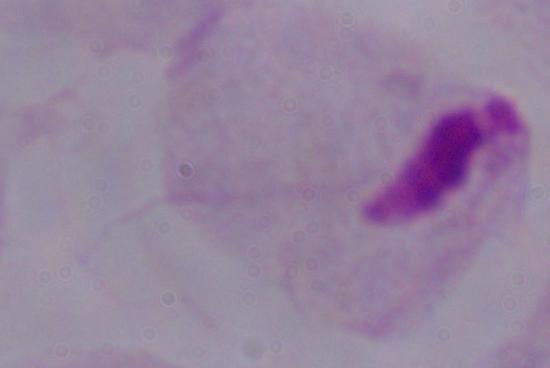
Summary:
  - Magnification: 1000x
  - Modality: photomicrograph
  - Identification: trichomonad